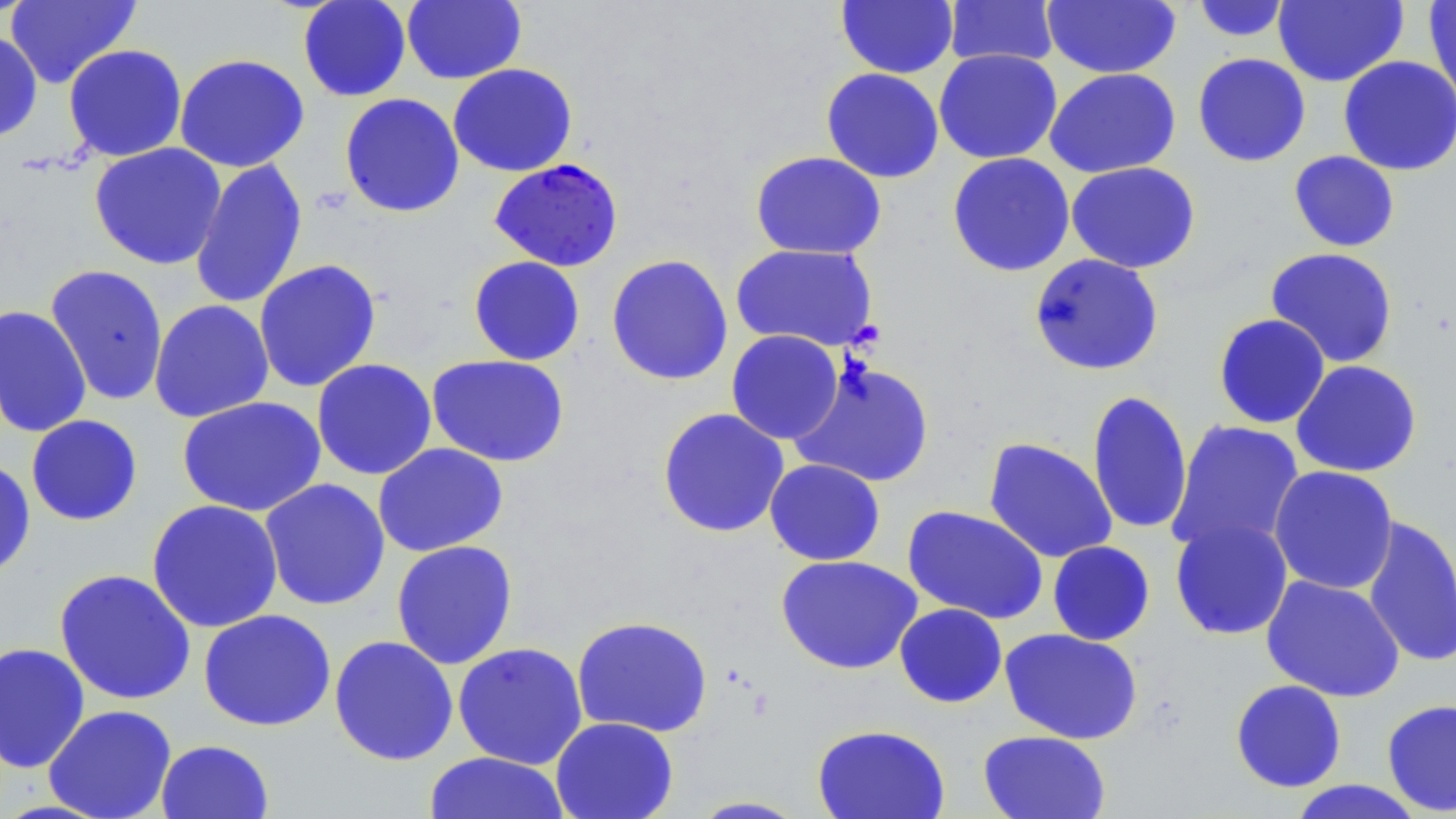 Approximate bounding boxes as [x1, y1, x2, y2] in pixels. Uninfected red blood cell locations: [5, 0, 141, 88], [297, 0, 412, 102], [1273, 0, 1408, 87], [1423, 0, 1455, 106], [401, 1, 526, 84], [836, 1, 958, 79], [943, 1, 1060, 69], [1042, 1, 1182, 78], [1191, 1, 1293, 43], [0, 29, 43, 144], [63, 44, 187, 162], [934, 48, 1062, 164], [174, 53, 310, 173], [1192, 53, 1311, 167], [1338, 55, 1456, 175], [447, 63, 578, 177], [821, 67, 944, 183], [1044, 68, 1181, 178], [339, 93, 465, 218], [89, 143, 227, 270], [750, 150, 887, 259], [1288, 151, 1400, 252], [947, 152, 1075, 277], [189, 158, 308, 310], [1065, 161, 1201, 273], [730, 243, 879, 351], [1264, 247, 1399, 368], [1029, 253, 1164, 376], [606, 254, 733, 386], [468, 256, 586, 365], [253, 259, 382, 393], [44, 264, 169, 406], [149, 299, 274, 422], [0, 305, 92, 438], [1213, 313, 1330, 429], [726, 329, 844, 444], [426, 354, 570, 467], [311, 358, 437, 480], [790, 359, 936, 489], [1291, 360, 1422, 478], [1086, 389, 1193, 536], [177, 396, 326, 517], [657, 407, 790, 538], [26, 414, 143, 526], [1166, 419, 1305, 557], [983, 437, 1118, 564], [372, 442, 508, 557], [0, 458, 37, 580], [764, 459, 885, 565], [1268, 465, 1399, 595], [259, 478, 391, 611], [146, 499, 284, 633], [902, 505, 1049, 625], [1360, 515, 1455, 668], [1169, 516, 1294, 640], [391, 540, 518, 670], [1047, 541, 1155, 645], [776, 554, 922, 675], [54, 568, 197, 705], [1261, 575, 1406, 702], [894, 603, 1008, 708], [198, 609, 336, 732], [571, 615, 713, 738], [999, 628, 1144, 745], [329, 635, 459, 766], [0, 642, 91, 772], [452, 642, 588, 770], [1230, 679, 1347, 792], [1381, 698, 1456, 815], [43, 704, 177, 819], [550, 716, 679, 819], [811, 723, 951, 819], [978, 730, 1111, 819], [155, 739, 274, 819], [423, 752, 571, 819], [1286, 780, 1428, 818], [687, 796, 810, 818]. Plasmodium falciparum-infected red blood cell locations: [488, 158, 624, 271]. Slide-level diagnosis: Plasmodium falciparum. May-Grünwald-Giemsa stain. Thin blood film. Image is 1456×819 pixels. One field of a larger specimen. Captured at 1000x magnification. Optical microscopy.